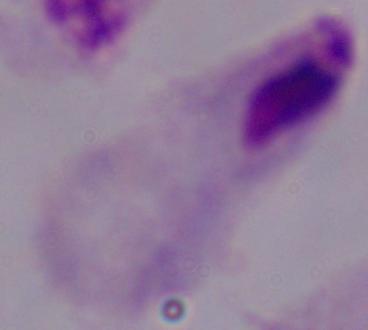
Micrograph. A trichomonad is shown. 1000x magnification.